Describe the morphology of the red blood cells.
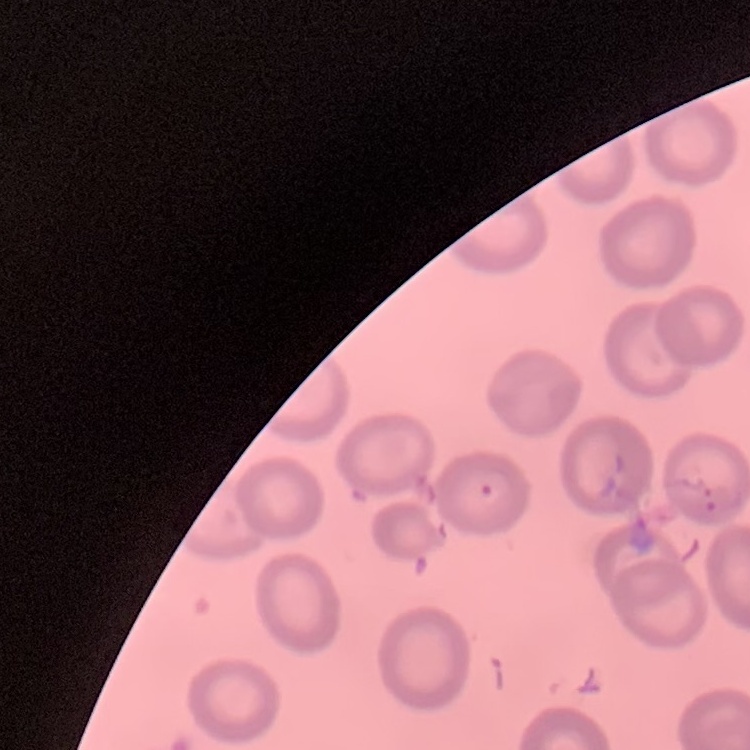
No rouleaux formation.

Summary:
  - Preparation: thin peripheral smear
  - Image type: square crop of a larger photomicrograph
  - Stain: Field's or Giemsa